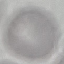 Result: negative for malaria parasites. Cell patch, automatically extracted from a larger field of view and resized to 64 × 64 pixels. Acquired by smartphone through the microscope eyepiece. Thin blood film. Giemsa stain.